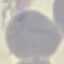
result = negative for malaria parasites
image type = automatically extracted cell patch, resized to 64 × 64 pixels
capture = smartphone camera at the microscope eyepiece
stain = Giemsa
preparation = thin blood smear